Point out every Plasmodium parasite.
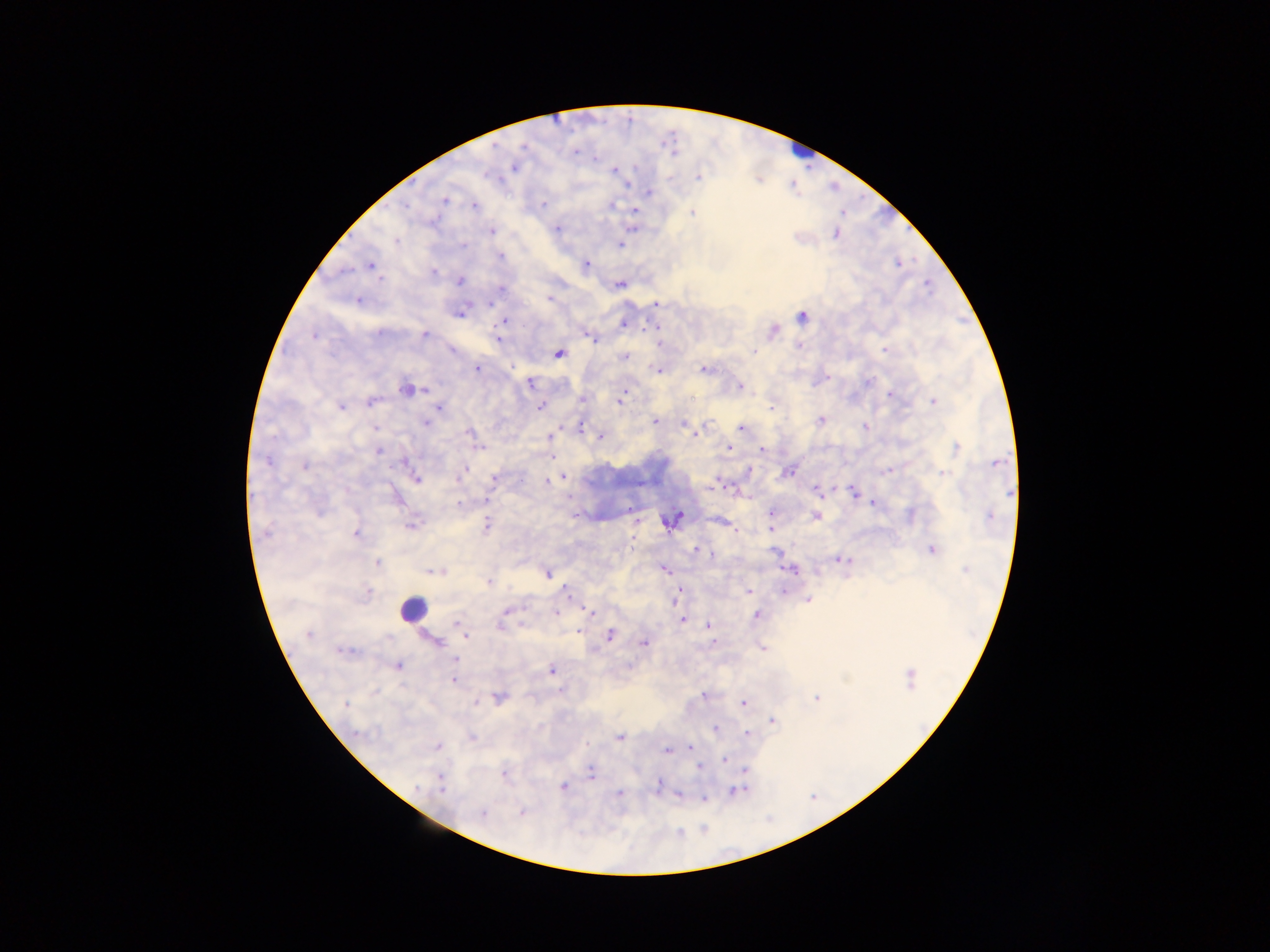

Approximate centers as [x, y] in pixels.
Plasmodium parasites: [574, 151], [593, 159], [514, 167], [614, 170], [698, 177], [628, 185], [649, 192], [445, 200], [543, 204], [611, 205], [406, 206], [474, 206], [634, 211], [692, 212], [433, 221], [557, 228], [492, 231], [835, 233], [397, 240], [462, 245], [620, 245], [500, 255], [586, 264], [370, 266], [433, 272], [379, 279], [459, 281], [620, 284], [502, 289], [549, 300], [358, 301], [490, 303], [656, 304], [459, 312], [801, 317], [503, 321], [624, 323], [655, 328], [774, 330], [377, 334], [314, 335], [424, 335], [589, 336], [497, 339], [799, 347], [886, 350], [453, 351], [755, 351], [559, 353], [624, 356], [478, 368], [656, 369], [704, 370], [828, 377], [530, 382], [869, 382], [739, 386], [405, 389], [424, 390], [890, 393], [582, 400], [619, 400], [370, 401], [933, 401], [539, 406], [341, 407], [438, 407], [772, 408], [820, 420], [654, 421], [425, 423], [685, 424], [865, 427], [375, 428], [581, 428], [741, 429], [690, 430], [469, 433], [696, 433], [550, 437], [600, 437], [729, 447], [956, 447], [479, 448], [761, 450], [378, 451], [553, 457], [267, 461], [997, 462], [305, 466], [465, 469], [890, 470], [460, 473], [789, 473], [944, 473], [494, 477], [563, 477], [416, 479], [547, 480], [457, 481], [713, 488], [816, 489], [854, 492], [1010, 492], [486, 501], [872, 503], [458, 505], [629, 507], [771, 512], [910, 515], [677, 516], [816, 516], [989, 516], [487, 524], [410, 526], [770, 529], [355, 534], [633, 540], [932, 549], [696, 550], [773, 551], [711, 554], [841, 559], [377, 563], [664, 569], [791, 569], [965, 571], [435, 572], [547, 574], [488, 581], [786, 588], [566, 589], [678, 592], [748, 592], [783, 592], [367, 593], [808, 600], [506, 611], [589, 612], [556, 613], [756, 616], [682, 620], [457, 624], [501, 624], [708, 626], [578, 633], [308, 634], [610, 635], [466, 636], [435, 641], [644, 643], [712, 643], [763, 648], [344, 651], [455, 659], [398, 666], [551, 670], [910, 678], [454, 681], [703, 696], [498, 698], [816, 698], [477, 702], [743, 703], [346, 704], [773, 721], [715, 728], [356, 733], [747, 734], [471, 738], [619, 738], [438, 746], [689, 747], [667, 750], [725, 760], [698, 766], [745, 770], [591, 772], [504, 776], [658, 785], [441, 786], [563, 786], [417, 787], [738, 791], [619, 794], [679, 795], [703, 798], [521, 812], [483, 813].

Summary:
  - Leukocyte locations: [804, 150], [411, 609]
  - Country: Ghana
  - Preparation: thick blood film
  - Field of view: single
  - Capture: mobile-phone photograph through a microscope
  - Image size: 1270×952 pixels